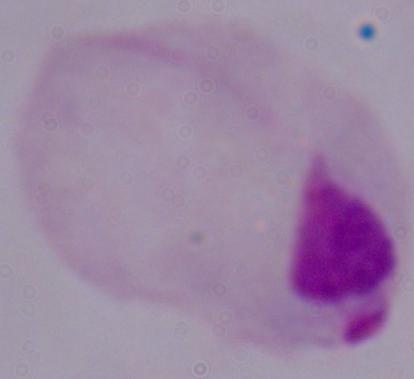

1000x magnification. Micrograph. A trichomonad is seen.